Locate every blood parasite and identify its species.
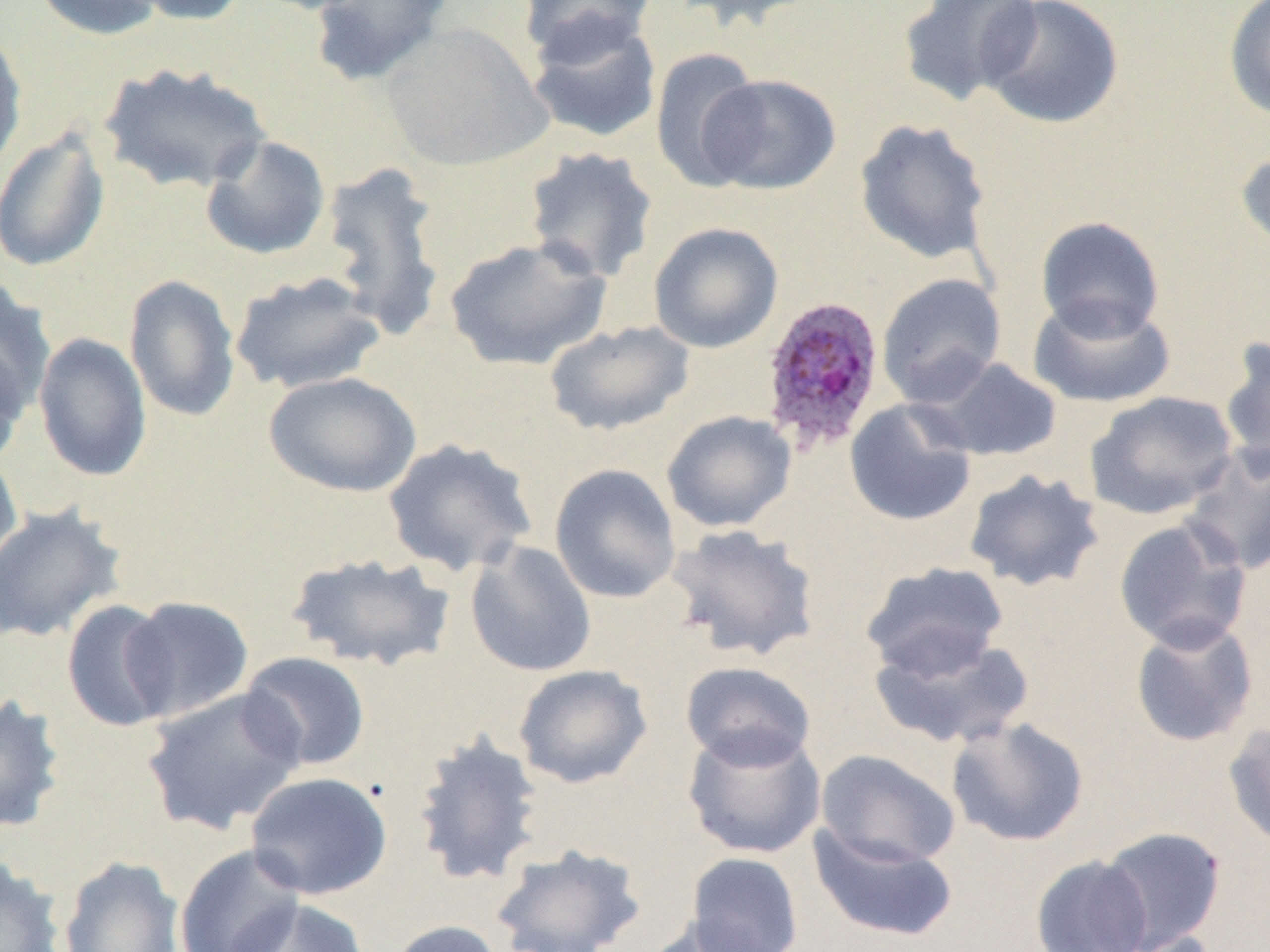

Approximate bounding boxes as [x1, y1, x2, y2] in pixels.
Plasmodium ovale-infected red blood cells: [758, 294, 885, 453].
No Plasmodium falciparum, Plasmodium malariae, Plasmodium vivax, Babesia divergens, or Trypanosoma brucei observed.

slide_level_diagnosis: Plasmodium ovale
modality: optical microscopy
field_of_view: single
preparation: thin blood film
magnification: 1000x
uninfected_red_blood_cell_locations: 'approximate bounding boxes as [x1, y1, x2, y2] in pixels: [30, 0, 167, 41], [122, 0, 251, 26], [247, 0, 376, 15], [309, 0, 453, 87], [518, 0, 657, 64], [669, 0, 822, 33], [897, 0, 1043, 107], [980, 0, 1125, 129], [1223, 0, 1270, 121], [525, 13, 663, 144], [380, 22, 552, 171], [0, 27, 27, 177], [650, 47, 765, 190], [98, 61, 272, 194], [700, 73, 841, 195], [854, 118, 992, 265], [0, 128, 111, 272], [200, 135, 331, 261], [1236, 146, 1270, 256], [522, 147, 659, 282], [318, 160, 449, 338], [1035, 216, 1165, 340], [648, 222, 783, 353], [442, 235, 612, 371], [230, 270, 387, 395], [876, 272, 1007, 405], [124, 274, 240, 423], [0, 277, 57, 417], [1028, 295, 1175, 407], [544, 320, 696, 436], [33, 333, 152, 482], [1218, 335, 1270, 473], [0, 339, 29, 469], [922, 356, 1063, 462], [264, 371, 421, 497], [1085, 390, 1239, 520], [844, 398, 977, 527], [661, 410, 797, 532], [382, 437, 539, 578], [1180, 443, 1270, 575], [0, 450, 23, 575], [549, 463, 682, 604], [963, 468, 1105, 592], [0, 504, 129, 643], [1112, 517, 1253, 652], [666, 523, 822, 662], [465, 541, 597, 677], [284, 552, 458, 673], [859, 561, 1009, 679], [119, 595, 254, 722], [61, 599, 177, 732], [1129, 616, 1259, 748], [868, 629, 1036, 750], [239, 651, 371, 772], [680, 660, 817, 770], [513, 664, 652, 789], [141, 687, 307, 836], [0, 694, 67, 834], [946, 716, 1089, 847], [1223, 719, 1270, 852], [681, 723, 827, 859], [411, 730, 546, 887], [815, 749, 961, 868], [245, 771, 393, 900], [807, 825, 960, 943], [1098, 826, 1227, 951], [489, 843, 647, 952], [174, 844, 306, 952], [686, 851, 804, 952], [1030, 854, 1154, 952], [0, 855, 66, 952], [58, 855, 185, 951], [223, 898, 370, 952], [638, 916, 780, 951], [385, 920, 505, 952], [1105, 930, 1222, 952]'
image_size: 1270×952 pixels